Classify this cell by malaria status.
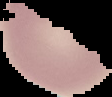

Uninfected.

Summary:
  - Image size: 112×97 pixels
  - Preparation: thin blood smear
  - Image type: cell region segmented out of the field of view; surrounding area masked to black